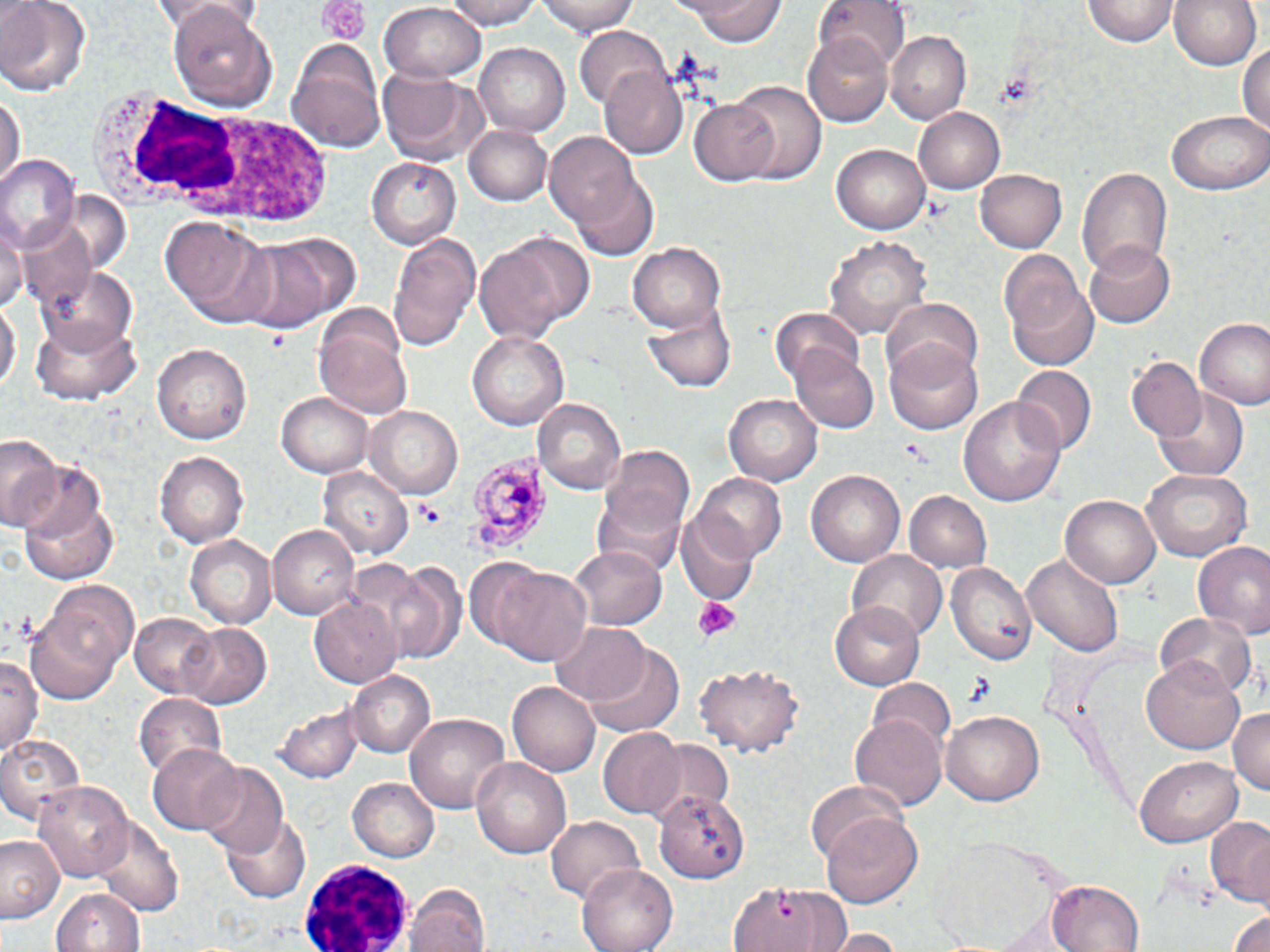
Approximate bounding boxes as (x1, y1, x2, y2) in pixels. Uninfected red blood cell locations: (0, 0, 91, 97), (147, 0, 244, 27), (444, 0, 541, 30), (539, 0, 638, 33), (679, 0, 784, 46), (817, 0, 911, 73), (1086, 0, 1180, 45), (1170, 0, 1261, 72), (166, 2, 278, 109), (378, 5, 485, 84), (577, 27, 672, 113), (803, 29, 892, 124), (885, 29, 971, 124), (1238, 38, 1268, 140), (289, 41, 386, 151), (475, 42, 569, 136), (378, 67, 489, 166), (598, 67, 687, 157), (726, 80, 826, 184), (0, 89, 23, 192), (687, 98, 782, 185), (914, 107, 1005, 193), (1168, 108, 1270, 196), (465, 124, 554, 205), (546, 134, 642, 230), (832, 142, 930, 230), (0, 155, 79, 251), (368, 157, 464, 248), (1077, 165, 1172, 282), (974, 170, 1069, 252), (571, 172, 658, 262), (161, 216, 274, 326), (1, 217, 25, 315), (17, 218, 97, 313), (245, 229, 359, 326), (475, 230, 593, 342), (387, 231, 482, 353), (824, 235, 932, 340), (1086, 241, 1176, 328), (628, 242, 727, 332), (998, 251, 1096, 372), (37, 263, 141, 355), (1, 291, 19, 403), (879, 299, 983, 390), (645, 301, 735, 394), (767, 307, 866, 388), (30, 317, 139, 404), (1195, 317, 1270, 410), (314, 325, 414, 420), (467, 332, 568, 431), (886, 339, 985, 434), (152, 342, 250, 447), (789, 344, 878, 434), (1127, 357, 1206, 441), (1012, 365, 1096, 454), (1154, 391, 1250, 482), (276, 392, 372, 476), (724, 392, 820, 485), (960, 392, 1067, 506), (532, 396, 627, 494), (364, 405, 467, 499), (0, 437, 61, 526), (593, 442, 696, 559), (0, 447, 98, 563), (155, 452, 246, 547), (1141, 467, 1250, 561), (322, 468, 412, 560), (806, 470, 907, 569), (694, 473, 785, 563), (15, 484, 120, 589), (904, 490, 991, 574), (1061, 493, 1162, 589), (678, 514, 756, 606), (267, 523, 358, 622), (185, 536, 277, 629), (1191, 542, 1270, 637), (569, 547, 666, 628), (1021, 549, 1123, 655), (848, 552, 946, 643), (351, 555, 456, 659), (948, 562, 1036, 667), (492, 566, 591, 665), (41, 582, 141, 679), (311, 595, 401, 688), (832, 602, 924, 690), (25, 610, 124, 706), (1155, 610, 1255, 697), (129, 613, 219, 699), (177, 621, 273, 709), (549, 621, 651, 708), (583, 643, 685, 738), (0, 654, 40, 756), (1145, 654, 1247, 753), (695, 664, 803, 755), (346, 670, 433, 757), (868, 678, 956, 750), (508, 682, 600, 776), (136, 692, 226, 782), (277, 703, 364, 782), (1229, 707, 1269, 796), (943, 709, 1041, 806), (405, 713, 511, 813), (849, 714, 946, 814), (597, 728, 686, 819), (0, 732, 88, 828), (637, 738, 733, 818), (148, 743, 244, 833), (1135, 756, 1243, 846), (471, 757, 570, 859), (198, 766, 288, 860), (348, 777, 438, 861), (808, 778, 915, 882), (35, 780, 135, 880), (655, 785, 751, 882), (223, 813, 312, 903), (823, 813, 923, 907), (94, 814, 185, 917), (544, 814, 646, 902), (1202, 819, 1270, 910), (0, 835, 64, 922), (930, 838, 1062, 949), (578, 861, 677, 951), (724, 875, 850, 952), (1048, 880, 1144, 952), (404, 882, 491, 952), (51, 888, 149, 952), (1226, 906, 1270, 952), (825, 929, 907, 951). Platelet locations: (318, 1, 369, 47), (264, 328, 288, 347), (901, 439, 931, 463), (416, 501, 443, 526), (693, 596, 740, 641), (965, 674, 994, 705). Plasmodium malariae-infected red blood cell locations: (473, 455, 559, 550). White blood cell locations: (101, 95, 342, 235), (292, 853, 410, 949). Slide-level diagnosis: Plasmodium malariae. Image is 1270×952 pixels. Optical microscopy. Thin blood smear. One field of a larger specimen. 1000x magnification. May-Grünwald-Giemsa stain.